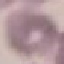
Summary:
  - Result: negative for malaria parasites
  - Preparation: thin smear
  - Image type: automatically extracted cell patch, resized to 64 × 64 pixels
  - Capture: smartphone camera at the microscope eyepiece
  - Stain: Giemsa